State the blood parasite species.
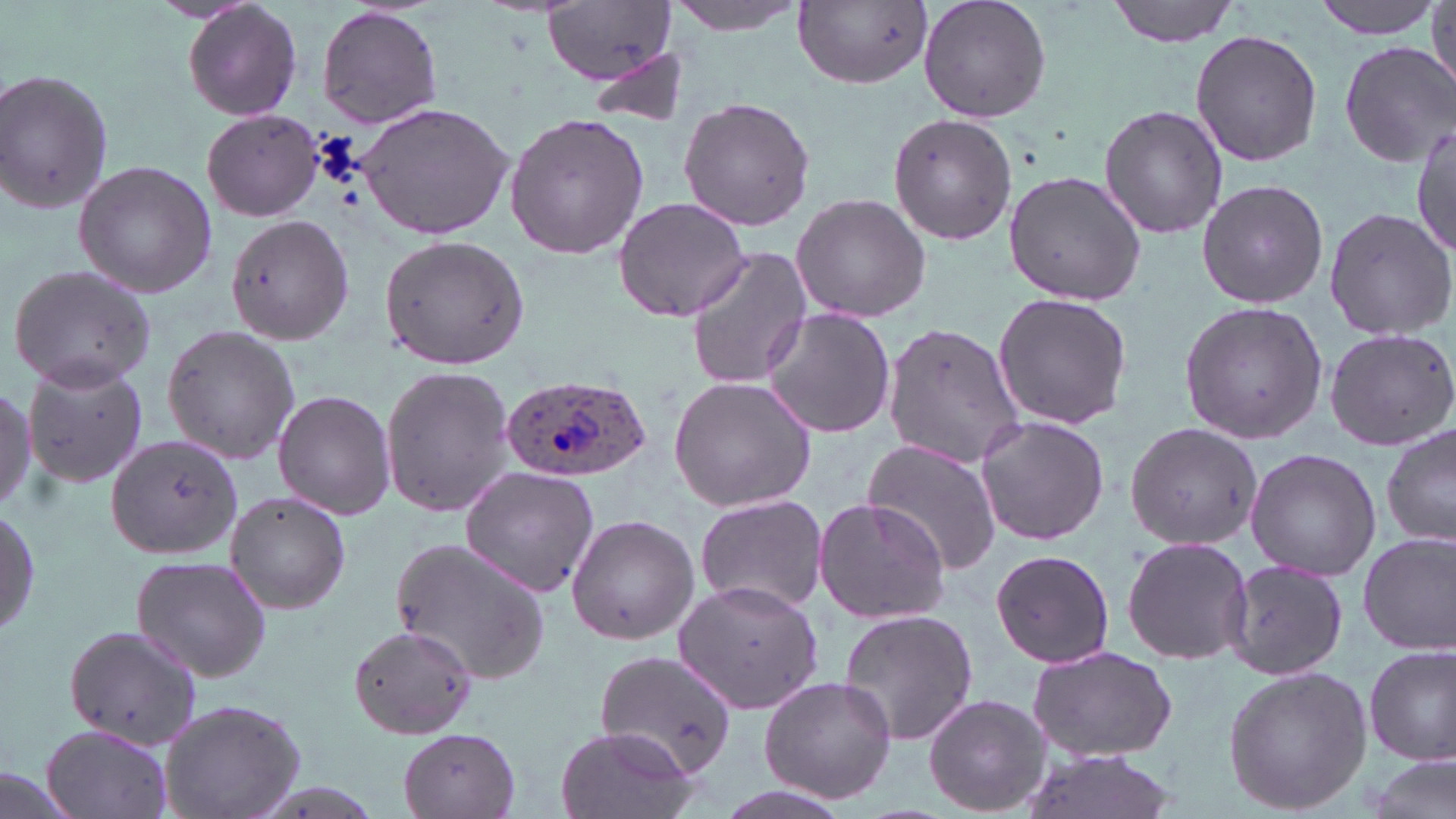
Plasmodium ovale.

Approximate bounding boxes as named x1/y1/x2/y2 corners in pixels. Uninfected red blood cell locations: (x1=183, y1=0, x2=303, y2=123), (x1=664, y1=0, x2=813, y2=35), (x1=796, y1=0, x2=932, y2=89), (x1=917, y1=0, x2=1052, y2=122), (x1=1107, y1=0, x2=1247, y2=46), (x1=1311, y1=0, x2=1441, y2=38), (x1=542, y1=2, x2=676, y2=85), (x1=1427, y1=4, x2=1456, y2=95), (x1=316, y1=6, x2=444, y2=130), (x1=1190, y1=28, x2=1322, y2=168), (x1=1338, y1=39, x2=1454, y2=169), (x1=584, y1=47, x2=692, y2=131), (x1=1, y1=66, x2=118, y2=219), (x1=676, y1=95, x2=815, y2=232), (x1=355, y1=100, x2=514, y2=240), (x1=1099, y1=102, x2=1229, y2=239), (x1=200, y1=109, x2=325, y2=222), (x1=504, y1=110, x2=651, y2=261), (x1=889, y1=113, x2=1017, y2=247), (x1=1413, y1=122, x2=1455, y2=261), (x1=73, y1=160, x2=217, y2=297), (x1=1003, y1=169, x2=1147, y2=307), (x1=1197, y1=177, x2=1328, y2=309), (x1=791, y1=192, x2=931, y2=323), (x1=611, y1=196, x2=751, y2=321), (x1=1323, y1=205, x2=1456, y2=341), (x1=225, y1=212, x2=353, y2=344), (x1=380, y1=235, x2=528, y2=371), (x1=685, y1=245, x2=812, y2=392), (x1=8, y1=263, x2=156, y2=390), (x1=990, y1=291, x2=1134, y2=431), (x1=1177, y1=301, x2=1328, y2=443), (x1=763, y1=308, x2=895, y2=438), (x1=883, y1=322, x2=1026, y2=470), (x1=160, y1=323, x2=300, y2=466), (x1=1323, y1=326, x2=1456, y2=453), (x1=22, y1=357, x2=149, y2=490), (x1=378, y1=365, x2=517, y2=517), (x1=669, y1=376, x2=817, y2=512), (x1=0, y1=383, x2=40, y2=516), (x1=272, y1=391, x2=396, y2=521), (x1=974, y1=416, x2=1109, y2=546), (x1=1126, y1=422, x2=1263, y2=549), (x1=1381, y1=422, x2=1456, y2=554), (x1=104, y1=432, x2=243, y2=561), (x1=861, y1=437, x2=1001, y2=577), (x1=1244, y1=449, x2=1382, y2=580), (x1=459, y1=465, x2=599, y2=595), (x1=224, y1=492, x2=351, y2=611), (x1=693, y1=494, x2=828, y2=616), (x1=813, y1=496, x2=951, y2=625), (x1=1, y1=505, x2=40, y2=642), (x1=565, y1=514, x2=699, y2=646), (x1=1356, y1=531, x2=1456, y2=655), (x1=392, y1=536, x2=555, y2=686), (x1=1120, y1=536, x2=1253, y2=665), (x1=990, y1=547, x2=1114, y2=670), (x1=129, y1=554, x2=274, y2=684), (x1=1220, y1=556, x2=1349, y2=679), (x1=675, y1=580, x2=826, y2=715), (x1=839, y1=607, x2=979, y2=748), (x1=62, y1=621, x2=203, y2=753), (x1=347, y1=623, x2=479, y2=740), (x1=1364, y1=644, x2=1455, y2=766), (x1=1027, y1=645, x2=1179, y2=762), (x1=598, y1=649, x2=740, y2=778), (x1=1222, y1=664, x2=1373, y2=817), (x1=757, y1=674, x2=897, y2=805), (x1=921, y1=694, x2=1051, y2=817), (x1=158, y1=697, x2=308, y2=819), (x1=397, y1=725, x2=524, y2=818), (x1=555, y1=725, x2=697, y2=819), (x1=39, y1=726, x2=174, y2=819), (x1=1021, y1=748, x2=1176, y2=819), (x1=1363, y1=754, x2=1453, y2=819), (x1=0, y1=763, x2=81, y2=819). Plasmodium ovale-infected red blood cell locations: (x1=498, y1=373, x2=652, y2=484). Image is 1456×819 pixels. 1000x magnification. Thin blood smear. Optical microscopy. May-Grünwald-Giemsa-stained preparation. One field of a larger specimen.